Report the malaria status.
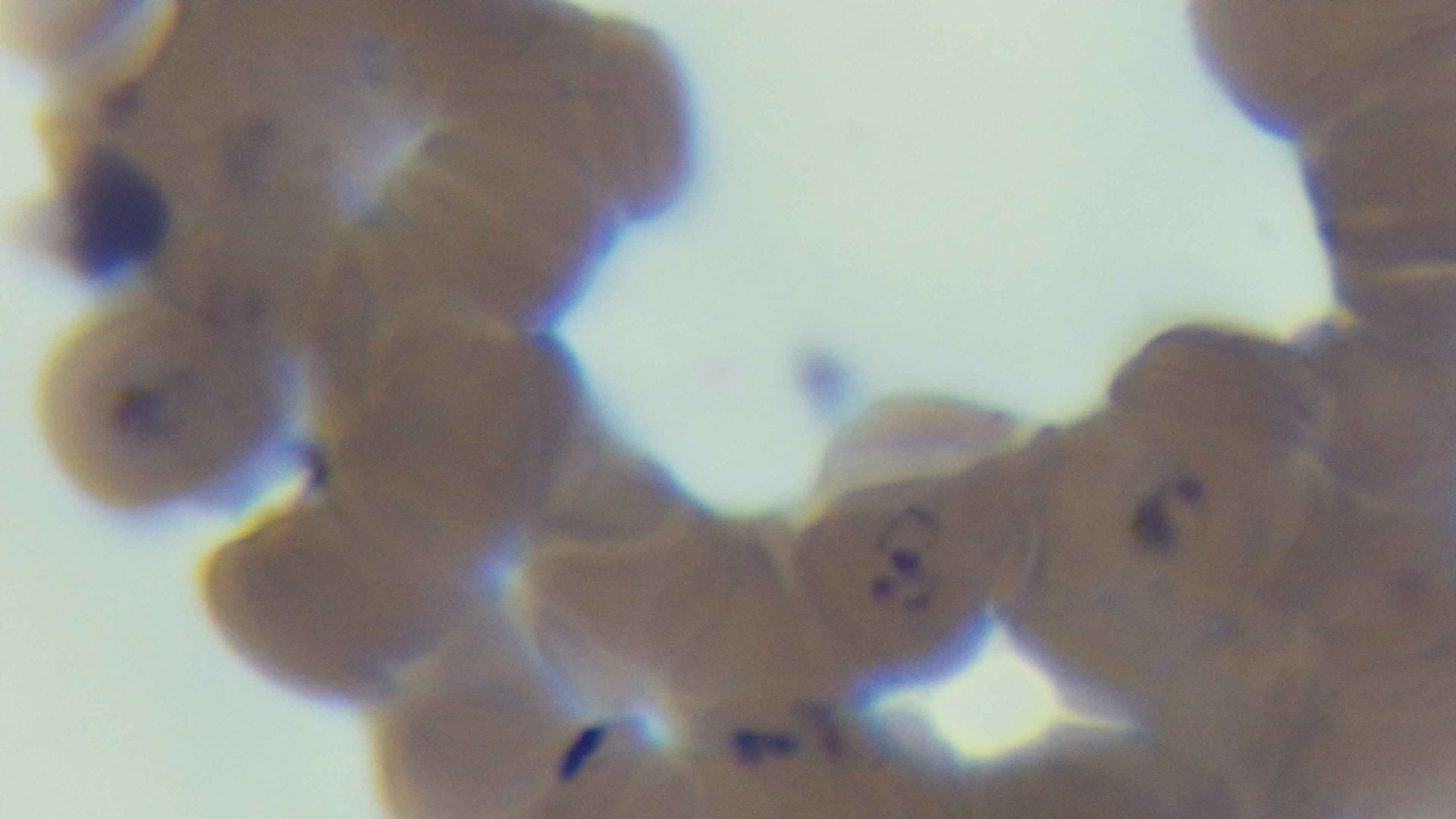

Positive.

Summary:
  - Objective: 100x oil immersion
  - Modality: light microscopy
  - Capture: mounted 4K digital camera
  - Field of view: one from the slide
  - Stain: Giemsa
  - Preparation: thin